Point out each malaria parasite.
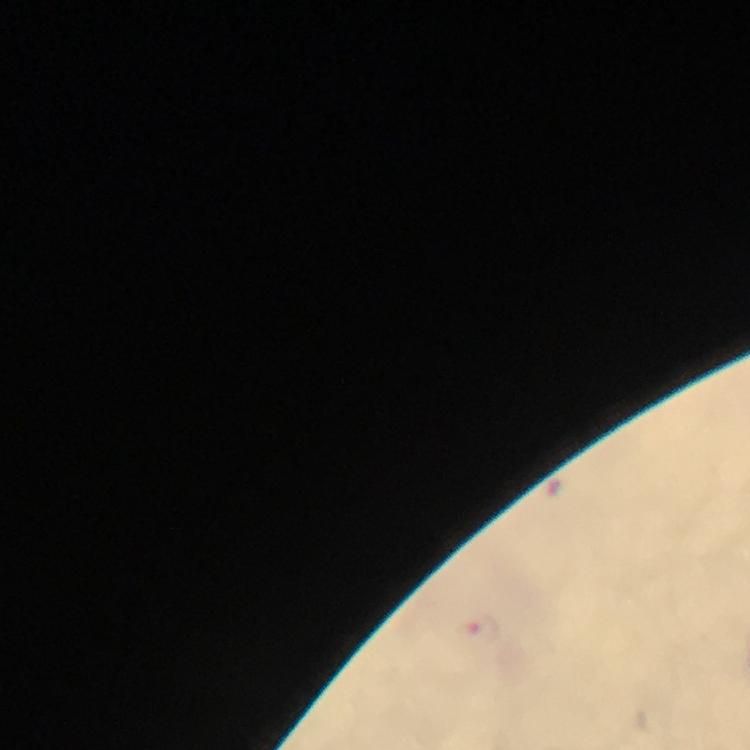

Approximate centers as [x, y] in pixels.
Malaria parasites: [484, 631].

stain = Giemsa
immersion oil = applied
magnification = 100x
preparation = thick blood smear
cropped from = one field of view
context = from a diagnostic examination for malaria
image size = 750×750 pixels
capture = smartphone mounted on the microscope